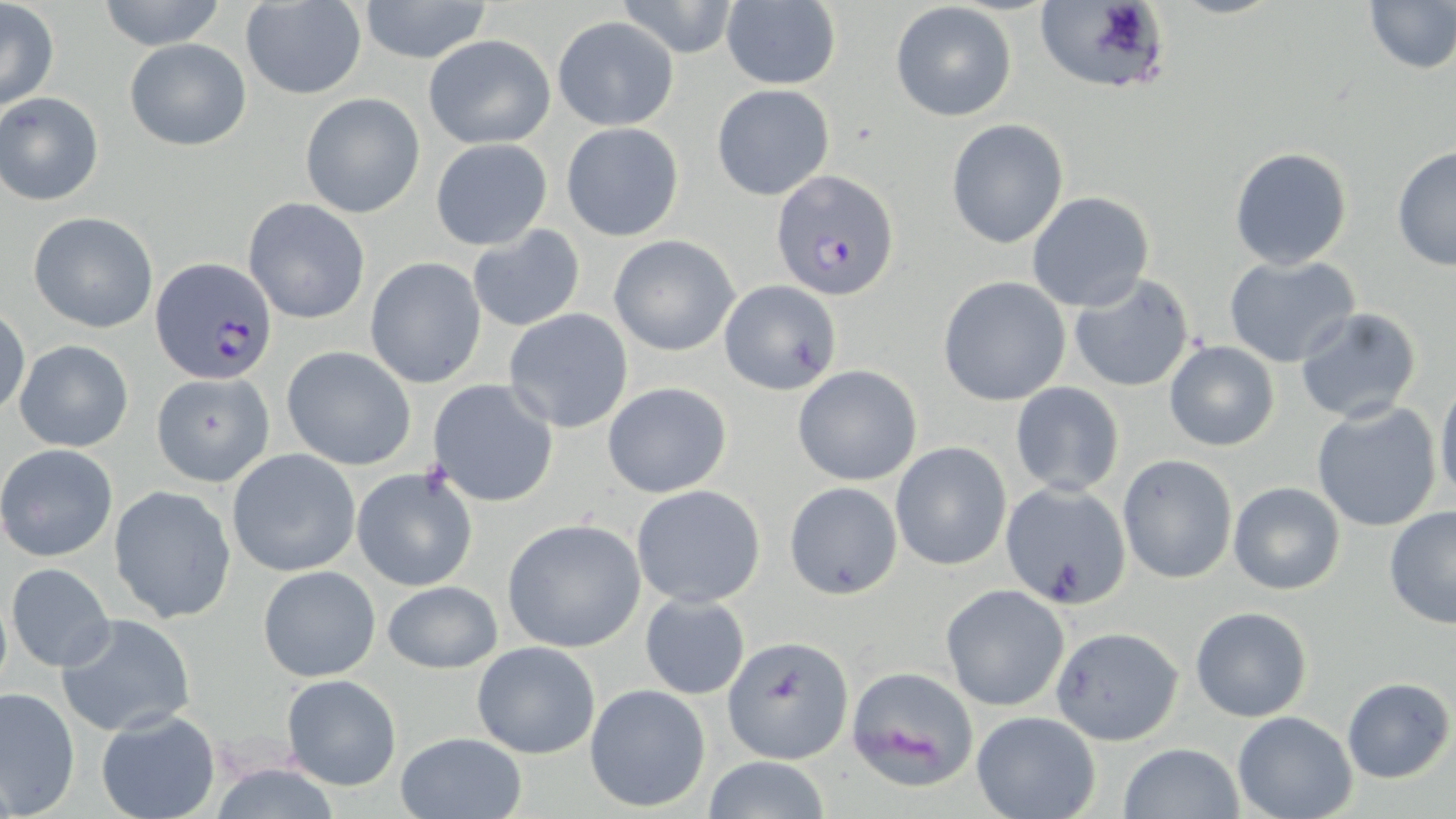
slide_level_diagnosis: Plasmodium falciparum
field_of_view: single
magnification: 1000x
uninfected_red_blood_cell_locations: 'approximate bounding boxes as (x1, y1, x2, y2) in pixels: (97, 0, 227, 51), (357, 0, 493, 64), (614, 0, 742, 58), (1361, 0, 1456, 74), (1, 1, 60, 111), (240, 2, 367, 99), (720, 2, 841, 89), (1033, 2, 1174, 97), (889, 3, 1017, 120), (551, 16, 679, 130), (424, 34, 556, 149), (123, 38, 252, 151), (711, 83, 834, 200), (1, 93, 103, 204), (300, 93, 425, 217), (946, 120, 1069, 249), (561, 122, 684, 241), (430, 138, 552, 250), (1390, 145, 1455, 272), (1229, 146, 1353, 271), (1027, 191, 1154, 312), (243, 199, 370, 324), (29, 211, 159, 333), (467, 225, 586, 332), (608, 235, 740, 355), (1224, 254, 1361, 368), (366, 257, 489, 388), (1067, 273, 1196, 394), (939, 275, 1071, 405), (718, 281, 842, 396), (1294, 306, 1423, 426), (1, 307, 30, 419), (502, 309, 634, 432), (14, 340, 134, 453), (1164, 341, 1281, 451), (281, 346, 417, 470), (793, 363, 923, 486), (149, 371, 273, 487), (1436, 376, 1456, 507), (427, 380, 559, 505), (602, 381, 732, 498), (1010, 382, 1124, 497), (1311, 403, 1443, 534), (890, 441, 1012, 571), (0, 444, 120, 563), (227, 448, 361, 576), (1118, 454, 1237, 583), (352, 465, 479, 593), (783, 482, 903, 600), (1003, 482, 1131, 608), (1228, 482, 1345, 595), (631, 484, 766, 607), (108, 485, 237, 624), (1384, 504, 1456, 631), (501, 518, 645, 652), (6, 561, 115, 672), (257, 564, 381, 681), (381, 580, 502, 674), (941, 585, 1070, 710), (640, 593, 750, 701), (1190, 606, 1312, 722), (56, 613, 195, 736), (1050, 626, 1184, 744), (722, 635, 853, 762), (471, 641, 601, 758), (847, 664, 983, 793), (280, 674, 402, 791), (1340, 677, 1453, 783), (585, 683, 713, 813), (1, 687, 79, 815), (96, 709, 220, 819), (971, 711, 1101, 819), (1233, 711, 1358, 819), (395, 731, 526, 819), (1119, 742, 1244, 819), (701, 756, 834, 819), (207, 760, 343, 819)'
plasmodium_falciparum_infected_red_blood_cell_locations: 'approximate bounding boxes as (x1, y1, x2, y2) in pixels: (772, 169, 900, 301), (150, 258, 277, 385)'
stain: May-Grünwald-Giemsa
modality: optical microscopy
preparation: thin blood smear
image_size: 1456×819 pixels